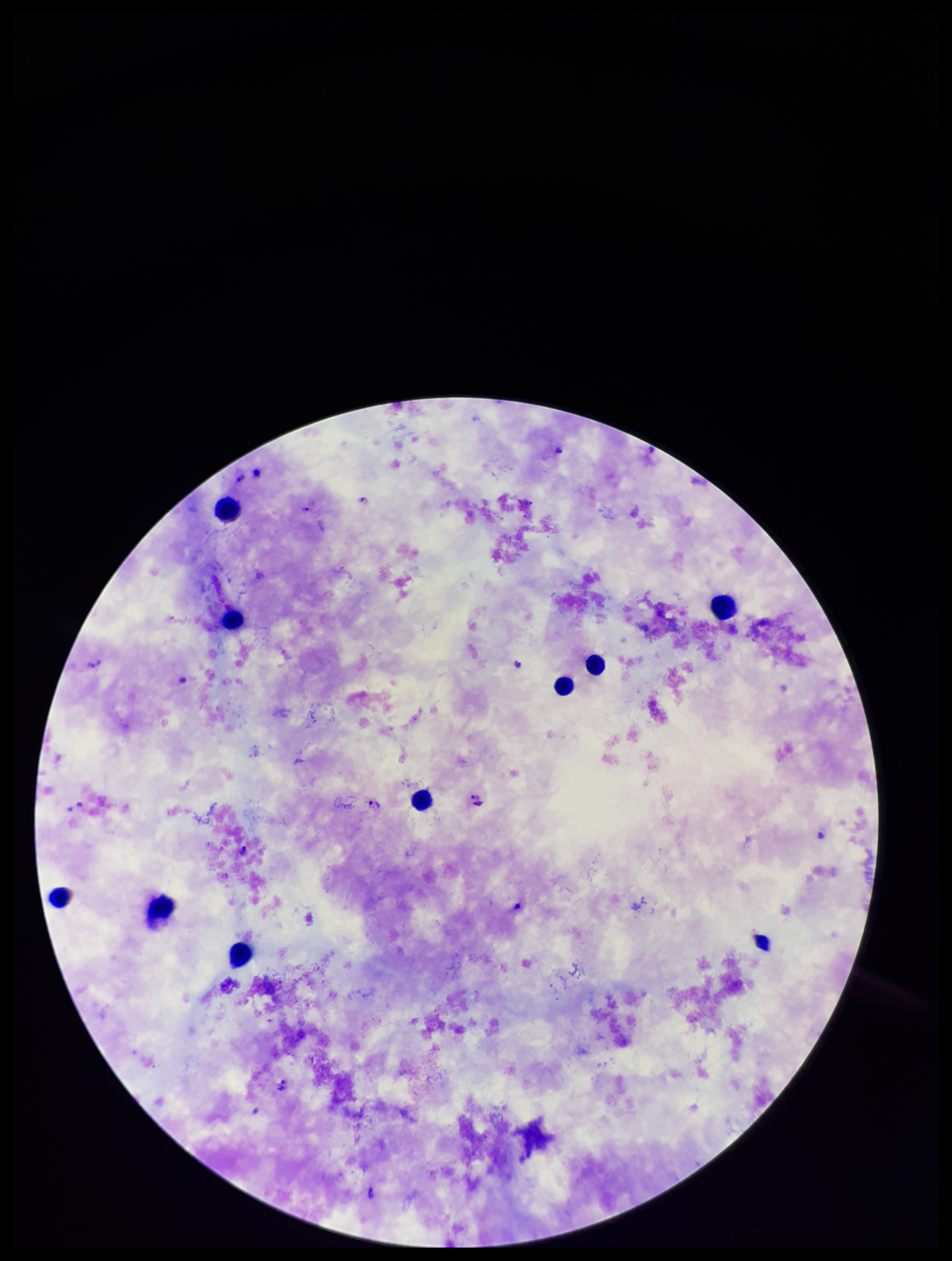
Leukocyte count: 9. Preparation: thick smear. Parasite count: 7. Species reported for this patient: Plasmodium falciparum. Plasmodium parasites: identified. Smartphone photograph taken through the eyepiece of a microscope. Giemsa stain. Patient malaria status: positive. Single field of view. Image is 952×1261 pixels.